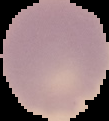

Summary:
  - Image type: cell region segmented out of the field of view; surrounding area masked to black
  - Result: no Plasmodium parasites seen
  - Image size: 109×121 pixels
  - Preparation: thin blood smear